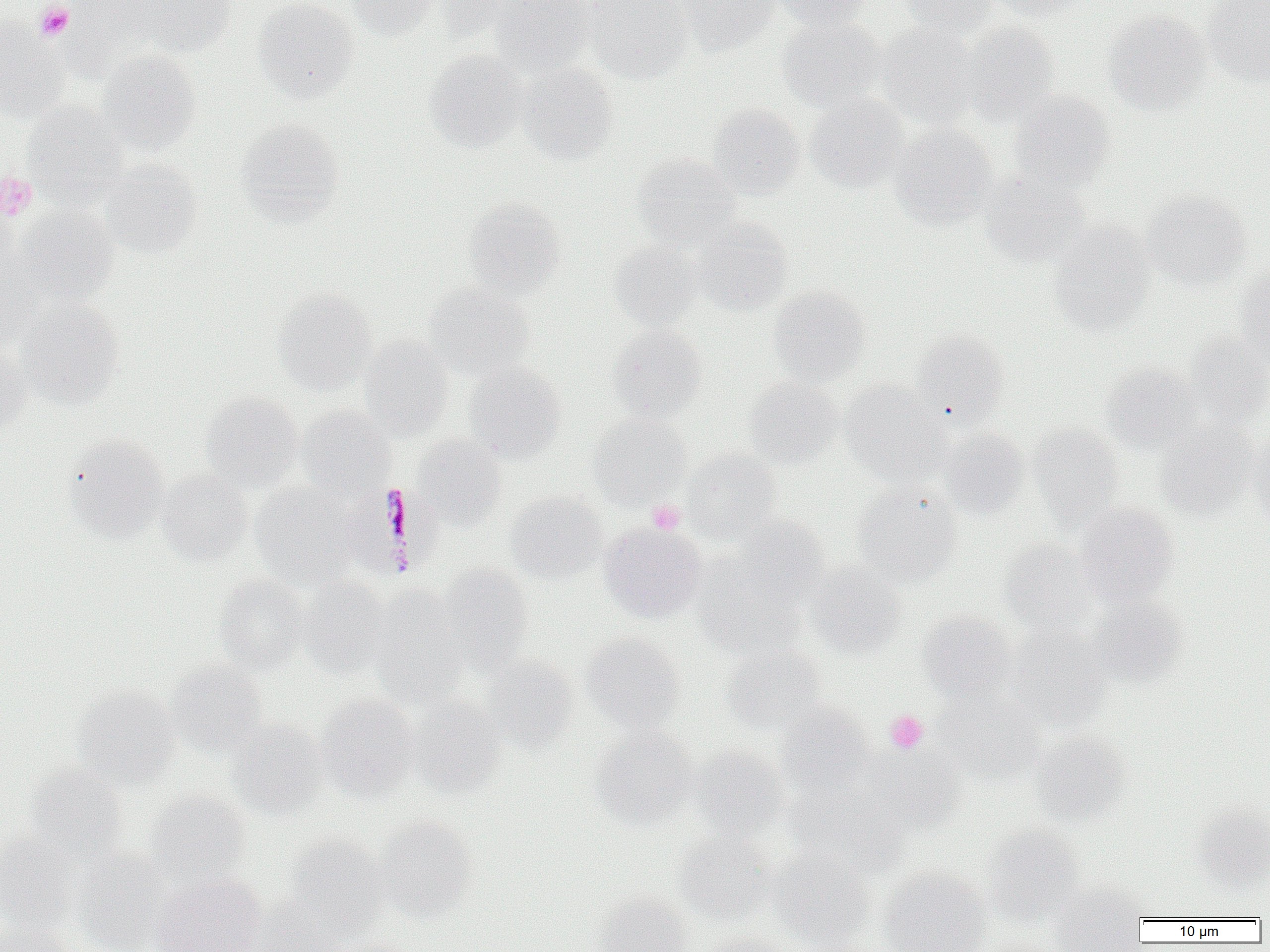
slide-level diagnosis = Plasmodium malariae
platelet locations = approximate bounding boxes as named x1/y1/x2/y2 corners in pixels: (x1=35, y1=2, x2=74, y2=41), (x1=0, y1=171, x2=37, y2=219), (x1=647, y1=500, x2=685, y2=534), (x1=885, y1=710, x2=929, y2=753)
uninfected red blood cell locations = approximate bounding boxes as named x1/y1/x2/y2 corners in pixels: (x1=59, y1=0, x2=156, y2=78), (x1=128, y1=0, x2=237, y2=57), (x1=252, y1=0, x2=359, y2=103), (x1=345, y1=0, x2=441, y2=39), (x1=432, y1=0, x2=533, y2=41), (x1=492, y1=0, x2=593, y2=75), (x1=580, y1=0, x2=693, y2=84), (x1=678, y1=0, x2=778, y2=56), (x1=772, y1=0, x2=873, y2=29), (x1=899, y1=0, x2=1000, y2=39), (x1=990, y1=0, x2=1087, y2=20), (x1=1203, y1=0, x2=1270, y2=87), (x1=1104, y1=10, x2=1212, y2=115), (x1=777, y1=17, x2=888, y2=112), (x1=0, y1=20, x2=68, y2=122), (x1=876, y1=22, x2=981, y2=128), (x1=959, y1=22, x2=1060, y2=125), (x1=96, y1=49, x2=202, y2=155), (x1=424, y1=50, x2=530, y2=152), (x1=519, y1=62, x2=619, y2=165), (x1=1010, y1=91, x2=1115, y2=192), (x1=805, y1=94, x2=909, y2=192), (x1=23, y1=101, x2=128, y2=202), (x1=708, y1=104, x2=806, y2=200), (x1=236, y1=119, x2=344, y2=223), (x1=890, y1=124, x2=998, y2=228), (x1=633, y1=154, x2=742, y2=251), (x1=101, y1=160, x2=202, y2=259), (x1=979, y1=171, x2=1089, y2=266), (x1=1142, y1=190, x2=1253, y2=289), (x1=0, y1=198, x2=19, y2=285), (x1=464, y1=198, x2=566, y2=298), (x1=13, y1=206, x2=119, y2=304), (x1=692, y1=218, x2=793, y2=314), (x1=1049, y1=223, x2=1155, y2=335), (x1=609, y1=243, x2=702, y2=330), (x1=0, y1=257, x2=49, y2=347), (x1=1234, y1=269, x2=1270, y2=372), (x1=422, y1=284, x2=534, y2=380), (x1=769, y1=285, x2=871, y2=386), (x1=273, y1=289, x2=378, y2=395), (x1=17, y1=299, x2=125, y2=408), (x1=607, y1=325, x2=707, y2=422), (x1=911, y1=328, x2=1009, y2=422), (x1=1184, y1=332, x2=1270, y2=427), (x1=359, y1=335, x2=454, y2=439), (x1=0, y1=343, x2=31, y2=437), (x1=465, y1=361, x2=566, y2=461), (x1=1100, y1=363, x2=1201, y2=453), (x1=744, y1=377, x2=842, y2=469), (x1=840, y1=381, x2=947, y2=483), (x1=201, y1=392, x2=303, y2=491), (x1=297, y1=406, x2=394, y2=497), (x1=588, y1=414, x2=691, y2=507), (x1=1157, y1=422, x2=1258, y2=519), (x1=1028, y1=424, x2=1123, y2=524), (x1=939, y1=428, x2=1030, y2=520), (x1=1248, y1=430, x2=1270, y2=527), (x1=64, y1=435, x2=170, y2=542), (x1=413, y1=435, x2=508, y2=528), (x1=682, y1=449, x2=782, y2=542), (x1=156, y1=469, x2=253, y2=565), (x1=250, y1=484, x2=358, y2=587), (x1=852, y1=486, x2=962, y2=586), (x1=506, y1=491, x2=608, y2=583), (x1=1075, y1=502, x2=1180, y2=606), (x1=736, y1=516, x2=829, y2=602), (x1=600, y1=522, x2=707, y2=622), (x1=999, y1=539, x2=1097, y2=635), (x1=693, y1=559, x2=806, y2=657), (x1=807, y1=562, x2=906, y2=658), (x1=437, y1=564, x2=534, y2=672), (x1=214, y1=575, x2=310, y2=675), (x1=298, y1=578, x2=393, y2=677), (x1=371, y1=587, x2=470, y2=706), (x1=1088, y1=595, x2=1186, y2=687), (x1=918, y1=611, x2=1016, y2=703), (x1=1008, y1=627, x2=1111, y2=731), (x1=581, y1=632, x2=685, y2=734), (x1=724, y1=645, x2=826, y2=734), (x1=480, y1=656, x2=579, y2=751), (x1=166, y1=661, x2=268, y2=757), (x1=74, y1=685, x2=181, y2=787), (x1=934, y1=691, x2=1044, y2=784), (x1=316, y1=693, x2=421, y2=799), (x1=410, y1=697, x2=507, y2=797), (x1=777, y1=703, x2=875, y2=796), (x1=227, y1=719, x2=327, y2=817), (x1=590, y1=727, x2=697, y2=830), (x1=1030, y1=733, x2=1132, y2=826), (x1=690, y1=745, x2=789, y2=840), (x1=864, y1=746, x2=965, y2=831), (x1=26, y1=765, x2=129, y2=861), (x1=788, y1=781, x2=908, y2=877), (x1=145, y1=790, x2=250, y2=885), (x1=1191, y1=802, x2=1270, y2=891), (x1=375, y1=816, x2=477, y2=921), (x1=982, y1=825, x2=1084, y2=923), (x1=674, y1=831, x2=777, y2=924), (x1=0, y1=832, x2=78, y2=932), (x1=285, y1=834, x2=389, y2=930), (x1=771, y1=847, x2=875, y2=950), (x1=73, y1=848, x2=173, y2=951), (x1=879, y1=867, x2=992, y2=952), (x1=151, y1=874, x2=265, y2=952), (x1=1051, y1=882, x2=1149, y2=951), (x1=592, y1=893, x2=692, y2=952), (x1=252, y1=895, x2=353, y2=951), (x1=0, y1=920, x2=72, y2=952), (x1=699, y1=931, x2=793, y2=952), (x1=326, y1=937, x2=415, y2=952)
field of view = one of a larger specimen
magnification = 1000x
image size = 1270×952 pixels
preparation = thin blood film
Plasmodium malariae-infected red blood cell locations = approximate bounding boxes as named x1/y1/x2/y2 corners in pixels: (x1=347, y1=483, x2=442, y2=579)
modality = light microscopy